Give the preparation type.
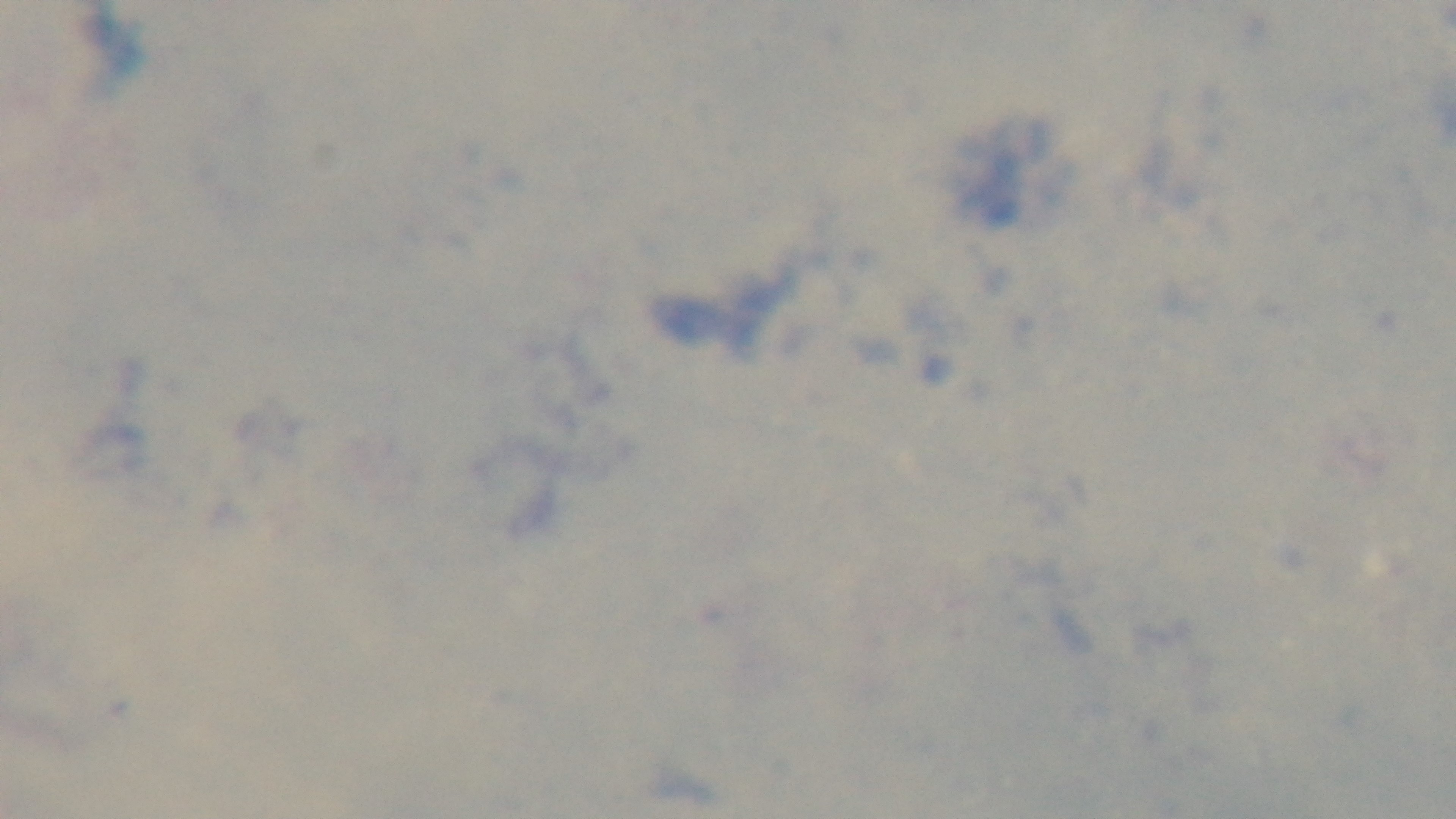

Thick.

Summary:
  - Objective: 100x oil immersion
  - Capture: mounted 4K digital camera
  - Malaria status: uninfected
  - Modality: light microscopy
  - Field of view: single
  - Stain: Giemsa